Give the extent of all uninfected red blood cells.
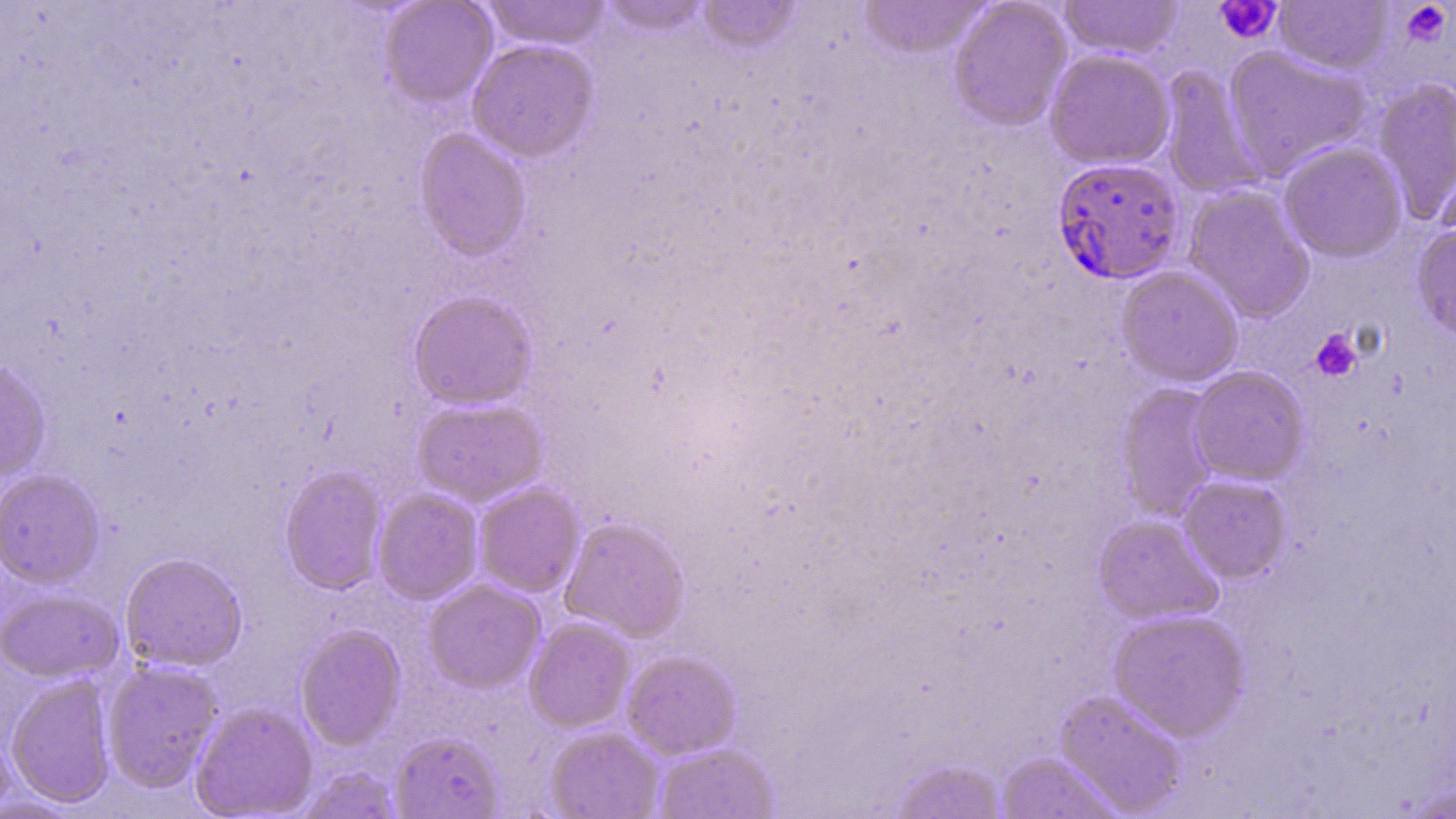
Approximate bounding boxes as (x1,y1)-(x2,y2) corner pairs in pixels.
Uninfected red blood cells: (482,0)-(612,51), (598,0)-(712,37), (859,0)-(990,59), (948,0)-(1072,132), (1058,0)-(1183,59), (379,1)-(498,110), (697,1)-(802,55), (1274,1)-(1392,75), (466,38)-(599,162), (1222,46)-(1372,179), (1044,49)-(1175,170), (1158,65)-(1267,200), (1372,77)-(1456,226), (414,127)-(532,261), (1279,142)-(1407,263), (1183,185)-(1315,324), (1412,222)-(1456,343), (1116,266)-(1244,388), (408,290)-(538,410), (0,357)-(51,482), (1189,366)-(1310,485), (1115,383)-(1222,522), (412,397)-(549,506), (279,464)-(388,595), (0,469)-(105,588), (1178,474)-(1292,583), (474,482)-(584,597), (372,488)-(484,605), (1093,515)-(1223,626), (559,516)-(690,642), (120,552)-(247,672), (423,578)-(545,693), (1,588)-(123,683), (1108,609)-(1250,742), (524,617)-(635,733), (295,625)-(406,750), (622,650)-(741,760), (102,660)-(223,792), (5,674)-(117,808), (1053,690)-(1188,817), (190,702)-(318,818), (545,725)-(664,819), (0,726)-(15,816), (390,731)-(503,818), (653,743)-(779,818), (996,752)-(1120,818), (890,757)-(1008,819), (299,764)-(401,819), (1401,782)-(1455,818).

Platelet locations: (1214,0)-(1282,44), (1400,2)-(1452,47), (1310,329)-(1363,382). Plasmodium falciparum-infected red blood cell locations: (1051,157)-(1184,285). Slide-level diagnosis: Plasmodium falciparum. Single field of view. Image is 1456×819 pixels. Thin blood smear. May-Grünwald-Giemsa stain. Light microscopy. Captured at 1000x magnification.